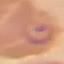

Result: malaria parasites identified. Thin smear of blood. Acquired by smartphone through the microscope eyepiece. Giemsa stain. Automatically extracted cell patch, resized to 64 × 64 pixels.